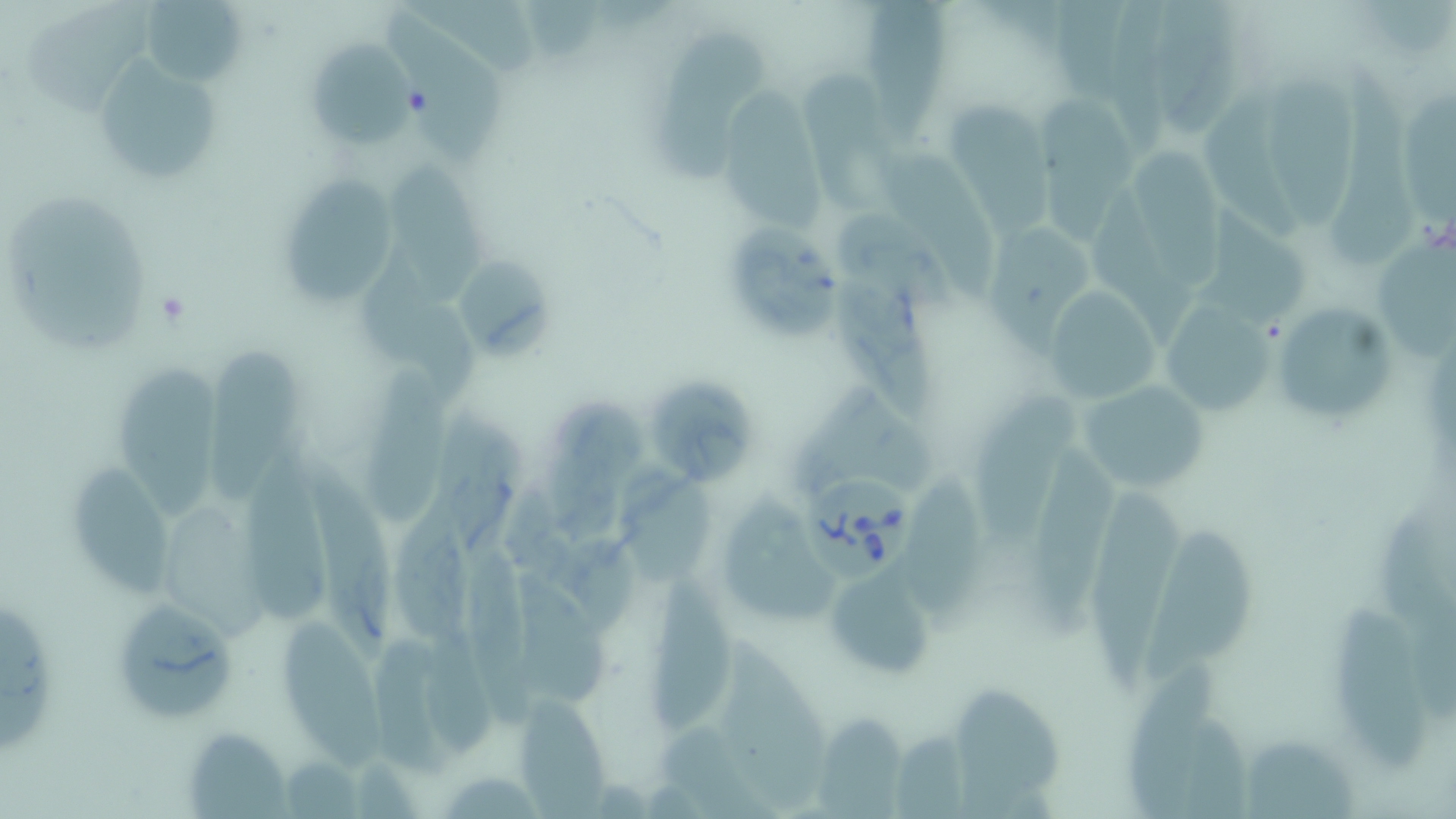 Approximate bounding boxes as named x1/y1/x2/y2 corners in pixels. Uninfected red blood cell locations: (x1=139, y1=0, x2=248, y2=88), (x1=1047, y1=0, x2=1125, y2=103), (x1=1150, y1=0, x2=1243, y2=132), (x1=850, y1=1, x2=954, y2=135), (x1=1108, y1=1, x2=1177, y2=145), (x1=25, y1=3, x2=153, y2=114), (x1=382, y1=10, x2=511, y2=167), (x1=651, y1=26, x2=774, y2=189), (x1=303, y1=37, x2=416, y2=147), (x1=93, y1=57, x2=227, y2=188), (x1=1340, y1=60, x2=1425, y2=271), (x1=799, y1=64, x2=889, y2=213), (x1=1262, y1=73, x2=1360, y2=231), (x1=1031, y1=94, x2=1136, y2=240), (x1=946, y1=97, x2=1052, y2=240), (x1=721, y1=98, x2=825, y2=226), (x1=1197, y1=101, x2=1310, y2=234), (x1=1132, y1=137, x2=1218, y2=285), (x1=881, y1=153, x2=1001, y2=306), (x1=383, y1=157, x2=482, y2=309), (x1=276, y1=174, x2=398, y2=306), (x1=2, y1=195, x2=154, y2=357), (x1=1084, y1=197, x2=1197, y2=347), (x1=836, y1=208, x2=959, y2=319), (x1=1206, y1=210, x2=1307, y2=327), (x1=985, y1=218, x2=1091, y2=356), (x1=731, y1=225, x2=842, y2=342), (x1=1370, y1=232, x2=1454, y2=362), (x1=457, y1=252, x2=552, y2=363), (x1=364, y1=253, x2=473, y2=409), (x1=833, y1=272, x2=941, y2=421), (x1=1040, y1=291, x2=1161, y2=405), (x1=1159, y1=293, x2=1283, y2=416), (x1=1282, y1=301, x2=1393, y2=420), (x1=204, y1=347, x2=303, y2=503), (x1=117, y1=364, x2=215, y2=522), (x1=361, y1=366, x2=453, y2=526), (x1=650, y1=374, x2=760, y2=488), (x1=1078, y1=380, x2=1211, y2=490), (x1=786, y1=381, x2=940, y2=496), (x1=977, y1=389, x2=1074, y2=555), (x1=540, y1=397, x2=649, y2=537), (x1=442, y1=408, x2=519, y2=563), (x1=1033, y1=444, x2=1117, y2=638), (x1=616, y1=459, x2=712, y2=588), (x1=244, y1=460, x2=326, y2=628), (x1=70, y1=461, x2=176, y2=599), (x1=305, y1=463, x2=394, y2=669), (x1=911, y1=470, x2=991, y2=629), (x1=506, y1=483, x2=641, y2=624), (x1=1092, y1=484, x2=1187, y2=687), (x1=392, y1=485, x2=474, y2=647), (x1=720, y1=489, x2=847, y2=625), (x1=1377, y1=496, x2=1452, y2=632), (x1=160, y1=500, x2=270, y2=641), (x1=1138, y1=530, x2=1267, y2=682), (x1=460, y1=544, x2=547, y2=731), (x1=518, y1=567, x2=614, y2=713), (x1=826, y1=568, x2=935, y2=679), (x1=649, y1=575, x2=735, y2=733), (x1=1328, y1=588, x2=1434, y2=777), (x1=109, y1=598, x2=239, y2=724), (x1=0, y1=600, x2=54, y2=757), (x1=272, y1=617, x2=393, y2=776), (x1=421, y1=623, x2=492, y2=754), (x1=715, y1=630, x2=832, y2=807), (x1=375, y1=636, x2=457, y2=780), (x1=1126, y1=659, x2=1212, y2=812), (x1=949, y1=684, x2=1061, y2=806), (x1=511, y1=693, x2=613, y2=812), (x1=809, y1=711, x2=910, y2=813), (x1=1177, y1=712, x2=1252, y2=818), (x1=182, y1=727, x2=291, y2=816), (x1=1247, y1=732, x2=1361, y2=819), (x1=892, y1=733, x2=971, y2=818), (x1=437, y1=772, x2=548, y2=816). Babesia divergens-infected red blood cell locations: (x1=794, y1=465, x2=925, y2=582). Platelet locations: (x1=402, y1=85, x2=433, y2=119). Slide-level diagnosis: Babesia divergens. Image is 1456×819 pixels. May-Grünwald-Giemsa stain. Thin blood film. One field of a larger specimen. 1000x magnification. Optical microscopy.